Outline each Plasmodium malariae-infected red blood cell.
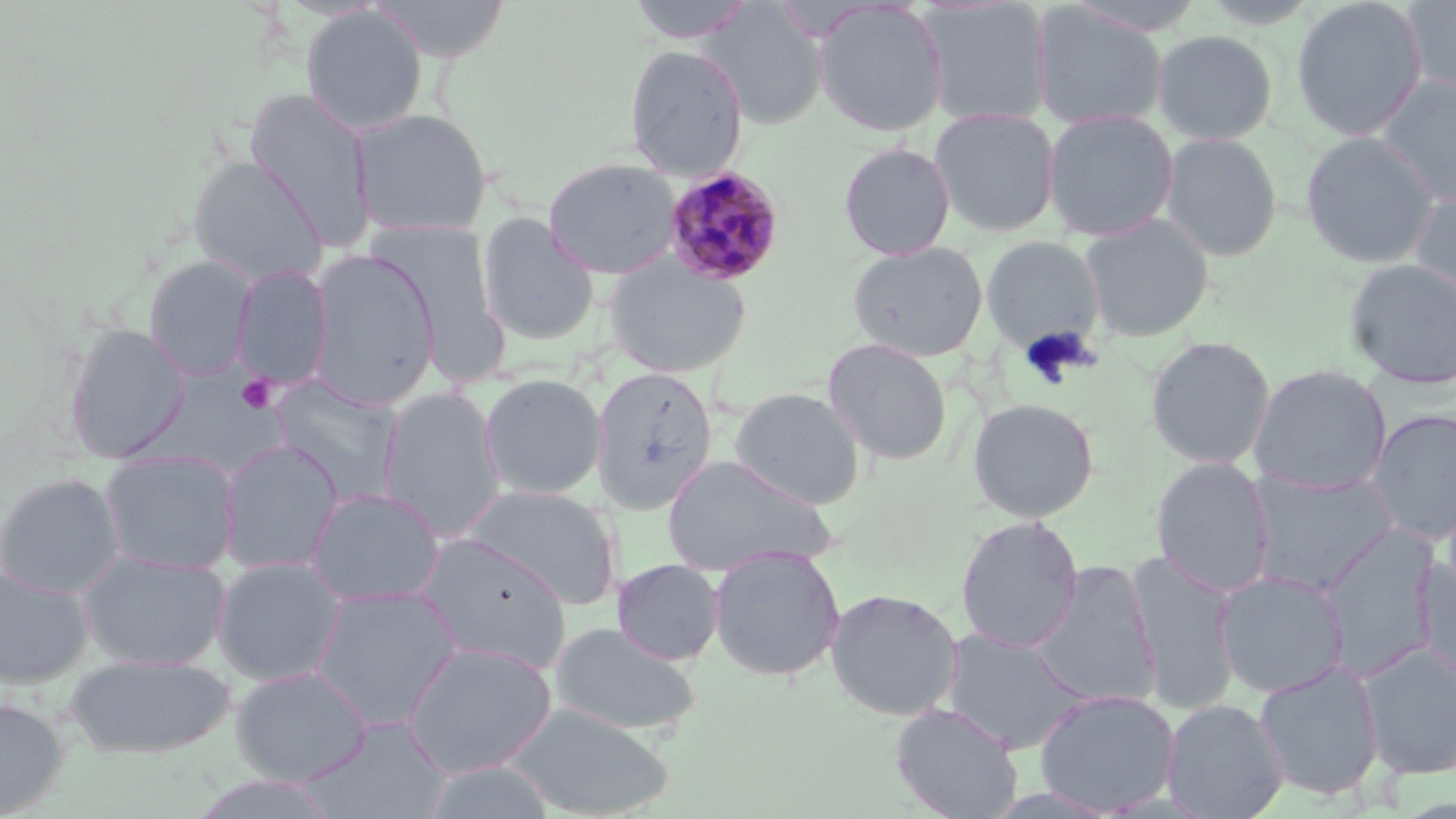
Approximate bounding boxes as named x1/y1/x2/y2 corners in pixels.
Plasmodium malariae-infected red blood cells: (x1=663, y1=167, x2=785, y2=287).

Platelet locations: (x1=236, y1=374, x2=278, y2=413). Uninfected red blood cell locations: (x1=366, y1=0, x2=513, y2=62), (x1=625, y1=0, x2=757, y2=42), (x1=1291, y1=0, x2=1428, y2=141), (x1=1400, y1=0, x2=1456, y2=98), (x1=813, y1=1, x2=949, y2=137), (x1=918, y1=1, x2=1053, y2=128), (x1=700, y1=2, x2=828, y2=129), (x1=1031, y1=3, x2=1169, y2=130), (x1=300, y1=6, x2=428, y2=135), (x1=1152, y1=29, x2=1278, y2=144), (x1=623, y1=44, x2=748, y2=179), (x1=1375, y1=74, x2=1456, y2=204), (x1=244, y1=88, x2=375, y2=252), (x1=353, y1=108, x2=492, y2=238), (x1=929, y1=108, x2=1061, y2=237), (x1=1042, y1=109, x2=1179, y2=242), (x1=1300, y1=131, x2=1440, y2=268), (x1=1158, y1=132, x2=1283, y2=262), (x1=838, y1=141, x2=956, y2=260), (x1=187, y1=156, x2=328, y2=285), (x1=543, y1=157, x2=682, y2=279), (x1=1408, y1=186, x2=1456, y2=312), (x1=477, y1=212, x2=599, y2=345), (x1=1079, y1=213, x2=1214, y2=342), (x1=369, y1=222, x2=511, y2=385), (x1=981, y1=236, x2=1105, y2=352), (x1=847, y1=241, x2=988, y2=361), (x1=307, y1=249, x2=440, y2=411), (x1=144, y1=254, x2=257, y2=381), (x1=605, y1=257, x2=751, y2=377), (x1=1344, y1=258, x2=1456, y2=390), (x1=231, y1=265, x2=334, y2=391), (x1=63, y1=323, x2=191, y2=462), (x1=1146, y1=336, x2=1276, y2=469), (x1=822, y1=337, x2=953, y2=465), (x1=1248, y1=364, x2=1392, y2=494), (x1=589, y1=365, x2=719, y2=514), (x1=479, y1=374, x2=607, y2=501), (x1=270, y1=376, x2=404, y2=504), (x1=378, y1=387, x2=507, y2=542), (x1=731, y1=387, x2=865, y2=510), (x1=967, y1=398, x2=1099, y2=521), (x1=1365, y1=408, x2=1456, y2=545), (x1=218, y1=439, x2=344, y2=574), (x1=99, y1=451, x2=240, y2=576), (x1=660, y1=454, x2=837, y2=576), (x1=1151, y1=456, x2=1275, y2=598), (x1=1246, y1=470, x2=1399, y2=595), (x1=0, y1=472, x2=124, y2=598), (x1=459, y1=485, x2=622, y2=609), (x1=305, y1=487, x2=445, y2=607), (x1=955, y1=514, x2=1084, y2=653), (x1=1315, y1=524, x2=1442, y2=682), (x1=414, y1=533, x2=574, y2=673), (x1=709, y1=547, x2=846, y2=681), (x1=78, y1=550, x2=231, y2=671), (x1=1126, y1=551, x2=1243, y2=714), (x1=1415, y1=555, x2=1456, y2=688), (x1=212, y1=557, x2=346, y2=686), (x1=612, y1=558, x2=725, y2=665), (x1=1030, y1=561, x2=1161, y2=709), (x1=0, y1=565, x2=94, y2=688), (x1=1213, y1=569, x2=1351, y2=699), (x1=308, y1=585, x2=463, y2=731), (x1=825, y1=588, x2=964, y2=720), (x1=548, y1=622, x2=702, y2=736), (x1=938, y1=627, x2=1089, y2=755), (x1=400, y1=641, x2=558, y2=778), (x1=1357, y1=642, x2=1456, y2=780), (x1=64, y1=654, x2=236, y2=758), (x1=1254, y1=661, x2=1385, y2=801), (x1=231, y1=666, x2=373, y2=785), (x1=1033, y1=688, x2=1180, y2=815), (x1=0, y1=698, x2=69, y2=816), (x1=1161, y1=698, x2=1289, y2=819), (x1=891, y1=701, x2=1023, y2=819), (x1=503, y1=702, x2=673, y2=818), (x1=298, y1=717, x2=451, y2=817), (x1=417, y1=759, x2=561, y2=819), (x1=189, y1=773, x2=345, y2=819). Slide-level diagnosis: Plasmodium malariae. Thin blood film. Optical microscopy. May-Grünwald-Giemsa stain. Image is 1456×819 pixels. Single field of view. Captured at 1000x magnification.